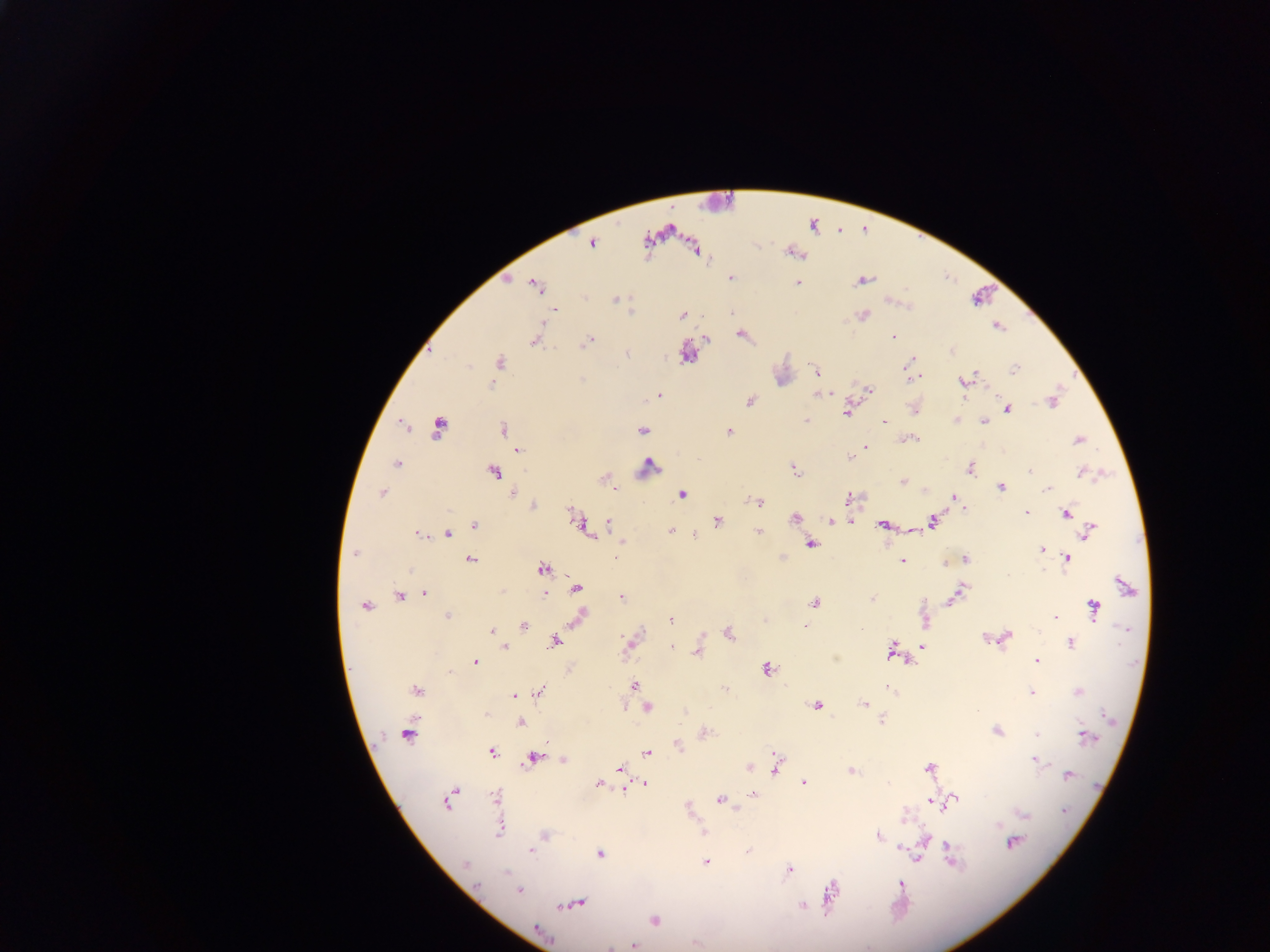 Approximate centers as (x, y) in pixels. Leukocyte locations: (718, 202), (647, 466). Plasmodium parasite locations: (812, 225), (591, 243), (694, 248), (792, 251), (730, 275), (507, 277), (862, 280), (796, 282), (535, 285), (614, 298), (682, 315), (862, 315), (997, 325), (741, 334), (892, 337), (705, 338), (536, 339), (587, 340), (951, 350), (685, 352), (908, 362), (499, 363), (1015, 368), (816, 372), (914, 376), (964, 381), (868, 390), (819, 393), (659, 395), (750, 401), (1052, 401), (913, 408), (1006, 409), (848, 411), (957, 419), (806, 421), (984, 421), (883, 422), (404, 427), (438, 428), (503, 430), (642, 430), (728, 432), (910, 438), (1077, 439), (866, 448), (518, 449), (848, 455), (396, 464), (793, 468), (969, 468), (492, 471), (1084, 472), (606, 478), (902, 482), (1000, 486), (613, 487), (1048, 488), (382, 493), (512, 493), (682, 494), (953, 496), (849, 499), (760, 501), (533, 505), (964, 509), (1026, 512), (1067, 512), (574, 514), (795, 516), (830, 520), (851, 520), (717, 521), (933, 521), (607, 523), (475, 525), (883, 525), (582, 526), (908, 528), (671, 530), (1089, 531), (758, 532), (419, 533), (446, 533), (590, 534), (694, 534), (622, 542), (811, 544), (1041, 548), (356, 553), (615, 558), (1066, 558), (470, 559), (782, 559), (965, 559), (902, 561), (543, 567), (1126, 587), (576, 588), (544, 592), (425, 593), (956, 595), (399, 596), (621, 596), (871, 597), (813, 603), (366, 606), (1093, 608), (447, 615), (581, 616), (1055, 617), (670, 620), (925, 620), (805, 626), (524, 627), (859, 629), (492, 630), (729, 632), (992, 638), (1003, 638), (555, 641), (1070, 642), (630, 644), (921, 645), (670, 646), (504, 647), (892, 650), (697, 651), (1036, 661), (475, 662), (766, 668), (634, 685), (726, 689), (888, 689), (416, 690), (540, 691), (1077, 692), (1032, 693), (513, 695), (817, 704), (863, 704), (646, 708), (686, 710), (520, 722), (997, 730), (407, 731), (703, 732), (1037, 734), (1084, 736), (677, 745), (492, 751), (646, 753), (534, 757), (563, 760), (1036, 760), (776, 766), (748, 767), (928, 768), (619, 769), (850, 771), (1067, 775), (622, 782), (599, 783), (645, 783), (804, 783), (624, 788), (754, 794), (496, 798), (449, 799), (719, 799), (951, 800), (942, 801), (932, 802), (687, 807), (1022, 813), (500, 828), (702, 832), (543, 835), (877, 835), (924, 840), (1012, 842), (902, 846), (530, 851), (748, 851), (598, 854), (916, 857), (950, 859), (706, 862), (466, 865), (789, 869), (900, 884), (518, 891), (831, 893), (575, 903), (802, 906), (654, 921), (538, 931), (632, 944). Sample from Ghana. Image is 1270×952 pixels. Single field of view. Thick blood smear. Mobile-phone photograph taken through the microscope.